Name the parasite shown.
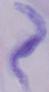
This is a trypanosome.

Photomicrograph. Captured at 1000x magnification.